Locate every blood parasite and identify its species.
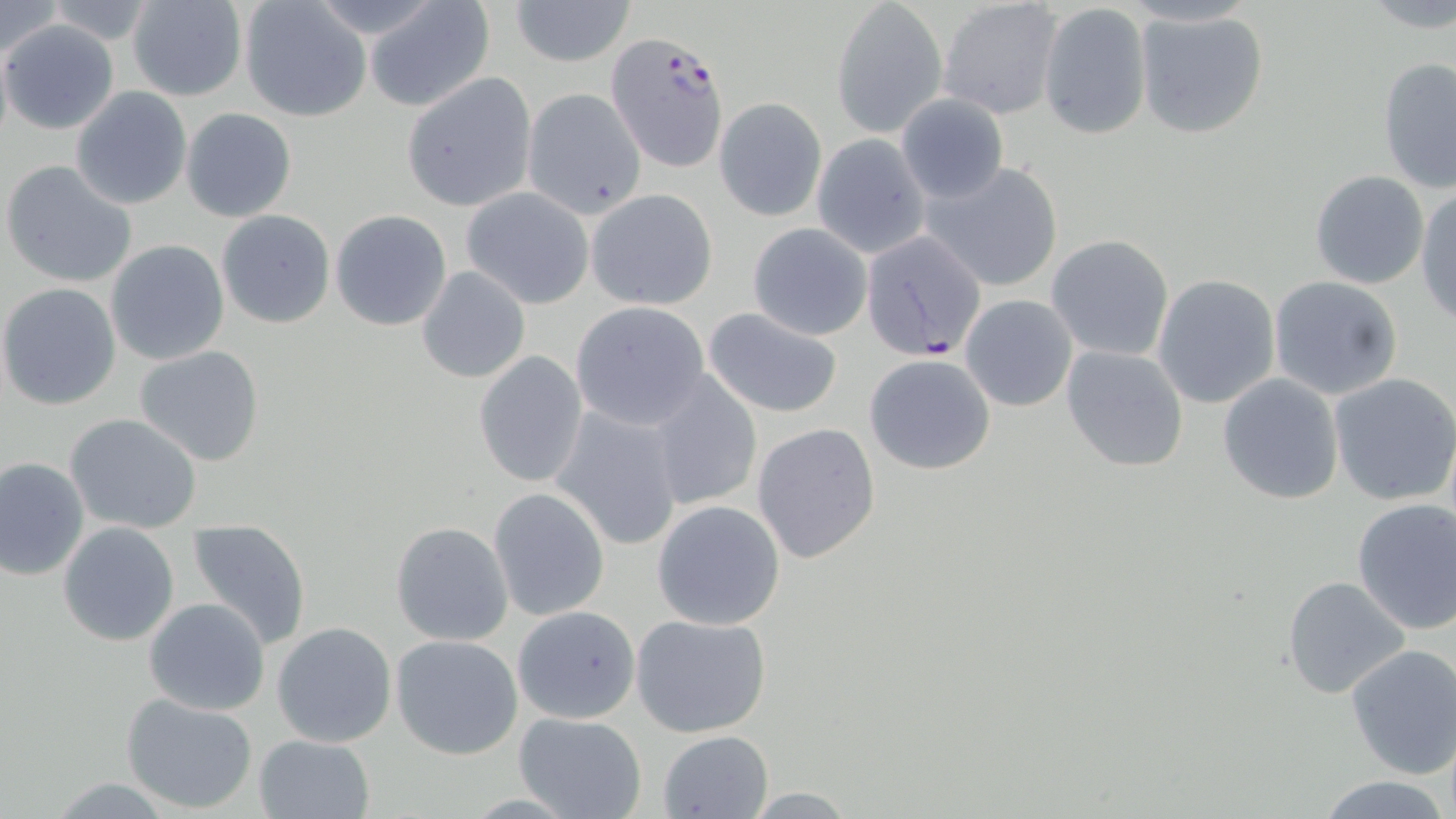
Approximate bounding boxes as [x1, y1, x2, y2] in pixels.
Plasmodium falciparum-infected red blood cells: [606, 31, 729, 172], [859, 232, 987, 360].
No Plasmodium ovale, Plasmodium malariae, Plasmodium vivax, Babesia divergens, or Trypanosoma brucei observed.

slide-level diagnosis = Plasmodium falciparum
image size = 1456×819 pixels
field of view = one of a larger specimen
magnification = 1000x
stain = May-Grünwald-Giemsa
modality = optical microscopy
uninfected red blood cell locations = approximate bounding boxes as [x1, y1, x2, y2] in pixels: [4, 0, 67, 59], [128, 0, 249, 102], [364, 0, 495, 112], [509, 0, 635, 69], [831, 1, 946, 138], [939, 1, 1063, 120], [42, 2, 155, 45], [1039, 2, 1154, 143], [237, 3, 369, 122], [1133, 8, 1273, 141], [2, 19, 120, 135], [0, 32, 13, 156], [1377, 56, 1456, 196], [401, 74, 538, 212], [69, 87, 193, 210], [521, 88, 647, 217], [897, 93, 1008, 204], [715, 97, 827, 221], [180, 108, 298, 223], [811, 135, 930, 259], [2, 159, 138, 287], [922, 161, 1065, 293], [1309, 169, 1430, 289], [1415, 186, 1456, 325], [463, 188, 594, 309], [586, 189, 718, 310], [216, 210, 335, 328], [330, 210, 452, 331], [746, 222, 874, 340], [1046, 236, 1174, 362], [105, 239, 229, 365], [416, 265, 531, 383], [1153, 273, 1281, 408], [1267, 274, 1404, 399], [0, 283, 121, 410], [959, 293, 1078, 412], [570, 301, 712, 430], [701, 307, 845, 419], [1059, 344, 1189, 472], [134, 346, 265, 466], [474, 351, 589, 489], [864, 353, 996, 476], [1216, 372, 1346, 505], [1326, 373, 1456, 506], [647, 374, 763, 513], [551, 405, 684, 550], [66, 413, 202, 534], [751, 421, 882, 564], [0, 457, 90, 583], [490, 489, 609, 621], [1351, 498, 1456, 635], [651, 501, 785, 630], [187, 518, 312, 650], [391, 521, 513, 647], [59, 522, 180, 646], [1281, 576, 1412, 702], [142, 598, 270, 716], [513, 605, 640, 724], [630, 613, 772, 738], [272, 622, 397, 749], [390, 634, 523, 759], [1344, 643, 1455, 779], [121, 693, 260, 811], [513, 712, 647, 819], [659, 730, 772, 817], [253, 733, 374, 818], [1314, 776, 1453, 818]
preparation = thin blood smear